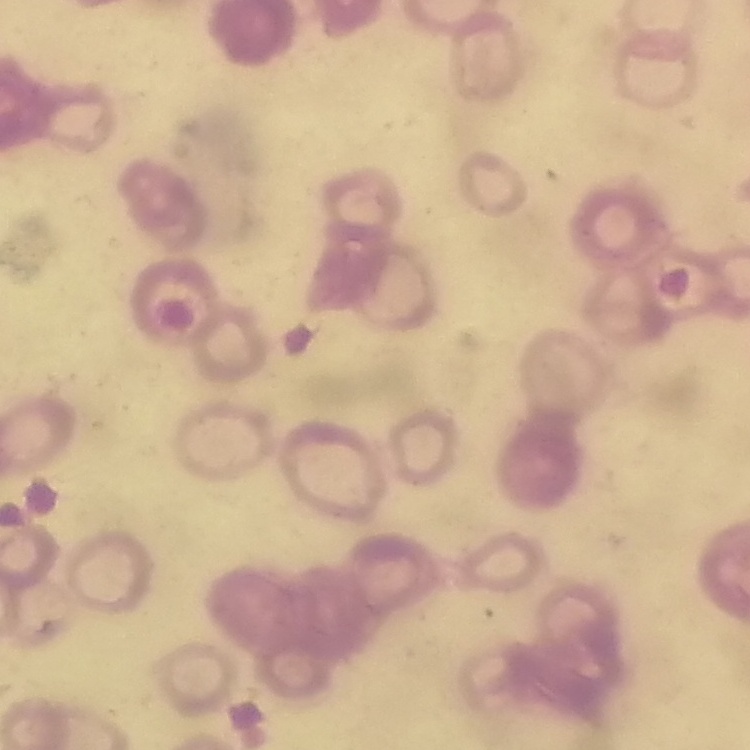

Summary:
  - Erythrocyte morphology: rouleaux formation
  - Stain: Field's or Giemsa
  - Preparation: thin peripheral smear
  - Image type: square crop of a larger photomicrograph